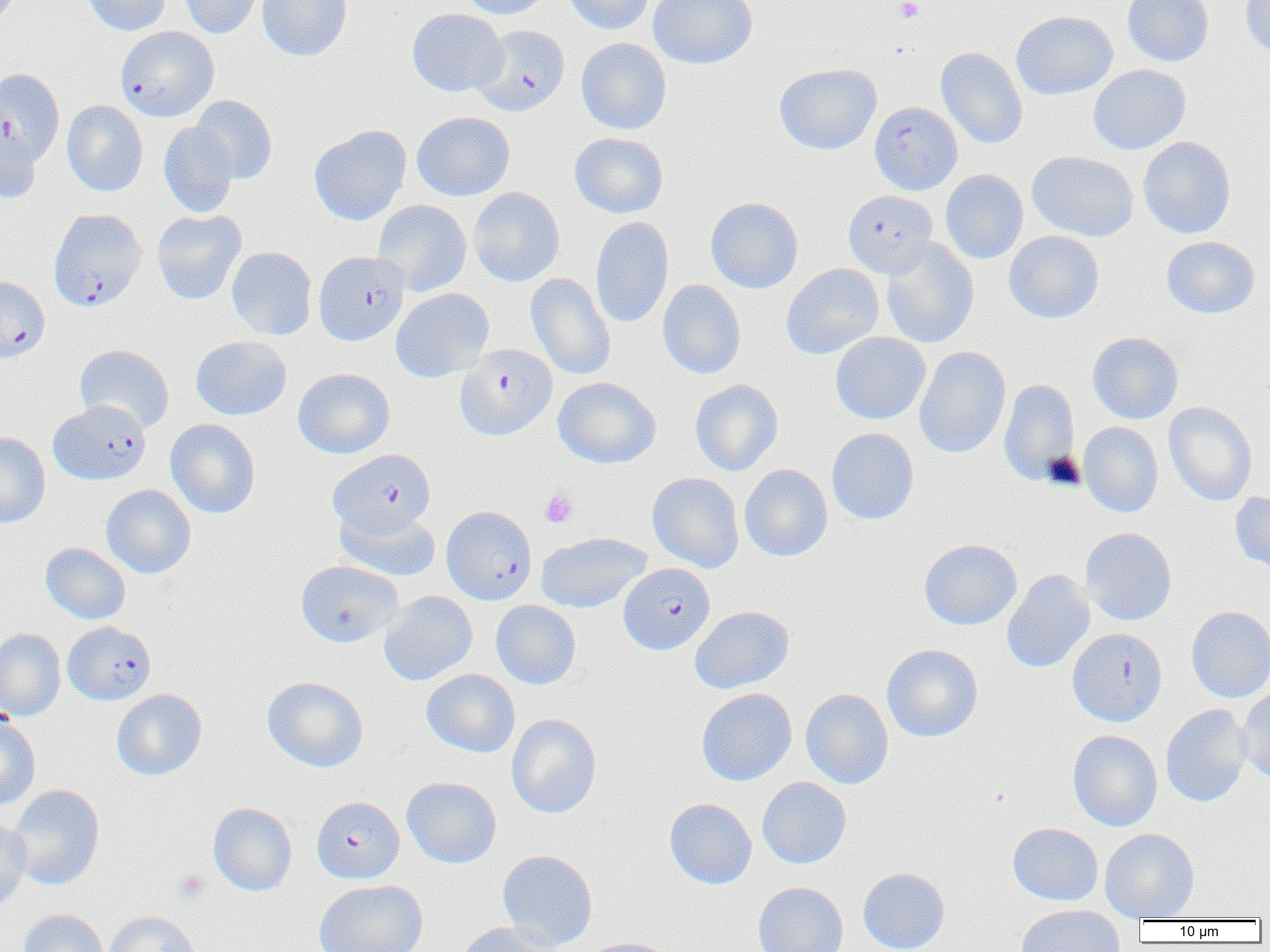

slide-level diagnosis = Plasmodium falciparum
preparation = thin blood film
modality = light microscopy
uninfected red blood cell locations = approximate bounding boxes as [x1, y1, x2, y2] in pixels: [82, 0, 171, 36], [179, 0, 265, 39], [258, 0, 352, 61], [455, 0, 553, 19], [563, 0, 656, 34], [647, 0, 758, 69], [1122, 0, 1214, 66], [1239, 1, 1270, 59], [407, 8, 507, 97], [1011, 11, 1117, 100], [575, 38, 672, 135], [936, 47, 1028, 149], [774, 63, 881, 154], [1088, 64, 1190, 154], [190, 95, 278, 184], [62, 100, 148, 196], [412, 111, 515, 201], [0, 116, 42, 204], [158, 123, 239, 218], [309, 124, 411, 225], [569, 132, 668, 218], [1138, 136, 1236, 239], [1026, 151, 1138, 242], [941, 169, 1028, 264], [469, 187, 565, 286], [705, 197, 803, 293], [373, 200, 472, 296], [151, 210, 247, 305], [591, 216, 674, 329], [1004, 231, 1104, 323], [1161, 236, 1260, 318], [876, 240, 979, 348], [226, 247, 317, 340], [781, 263, 884, 359], [526, 272, 616, 380], [657, 280, 746, 379], [391, 288, 494, 382], [831, 332, 931, 424], [1087, 332, 1183, 424], [190, 336, 291, 420], [74, 344, 174, 433], [913, 346, 1011, 458], [293, 368, 395, 458], [553, 377, 661, 468], [690, 379, 783, 476], [999, 379, 1079, 486], [1164, 402, 1257, 505], [165, 419, 261, 518], [1079, 422, 1163, 517], [826, 427, 920, 525], [0, 432, 51, 528], [739, 464, 833, 561], [648, 472, 744, 573], [101, 484, 196, 578], [1230, 491, 1270, 575], [334, 506, 441, 581], [1080, 527, 1177, 625], [536, 532, 651, 614], [918, 538, 1022, 630], [40, 542, 131, 624], [295, 560, 403, 647], [1001, 569, 1096, 673], [379, 591, 477, 686], [491, 600, 581, 690], [689, 606, 794, 694], [1186, 606, 1270, 702], [0, 628, 66, 721], [882, 643, 983, 743], [421, 669, 520, 758], [262, 676, 368, 772], [1237, 686, 1270, 784], [696, 687, 797, 786], [801, 688, 893, 789], [111, 689, 207, 781], [1160, 704, 1253, 807], [506, 713, 601, 819], [0, 715, 41, 812], [1067, 729, 1162, 831], [402, 776, 502, 868], [757, 777, 852, 869], [6, 784, 106, 890], [664, 798, 757, 889], [208, 802, 298, 896], [0, 817, 31, 911], [1008, 822, 1104, 906], [1099, 828, 1199, 921], [497, 849, 598, 951], [858, 867, 950, 952], [313, 880, 428, 952], [753, 881, 848, 952], [1015, 904, 1125, 952], [18, 909, 109, 952], [103, 911, 201, 952], [455, 922, 560, 952], [579, 937, 677, 952]
field of view = single
magnification = 1000x
platelet locations = approximate bounding boxes as [x1, y1, x2, y2] in pixels: [895, 0, 924, 23], [540, 489, 578, 528], [174, 870, 208, 902]
image size = 1270×952 pixels
Plasmodium falciparum-infected red blood cell locations = approximate bounding boxes as [x1, y1, x2, y2] in pixels: [474, 25, 570, 116], [115, 26, 219, 121], [0, 67, 65, 166], [869, 101, 963, 195], [848, 192, 942, 280], [48, 208, 147, 311], [314, 251, 409, 346], [0, 275, 50, 362], [455, 344, 557, 441], [48, 400, 151, 485], [328, 449, 436, 538], [441, 505, 537, 604], [618, 563, 715, 654], [62, 621, 156, 706], [1067, 628, 1167, 726], [312, 796, 405, 883]